Locate and identify every blood parasite.
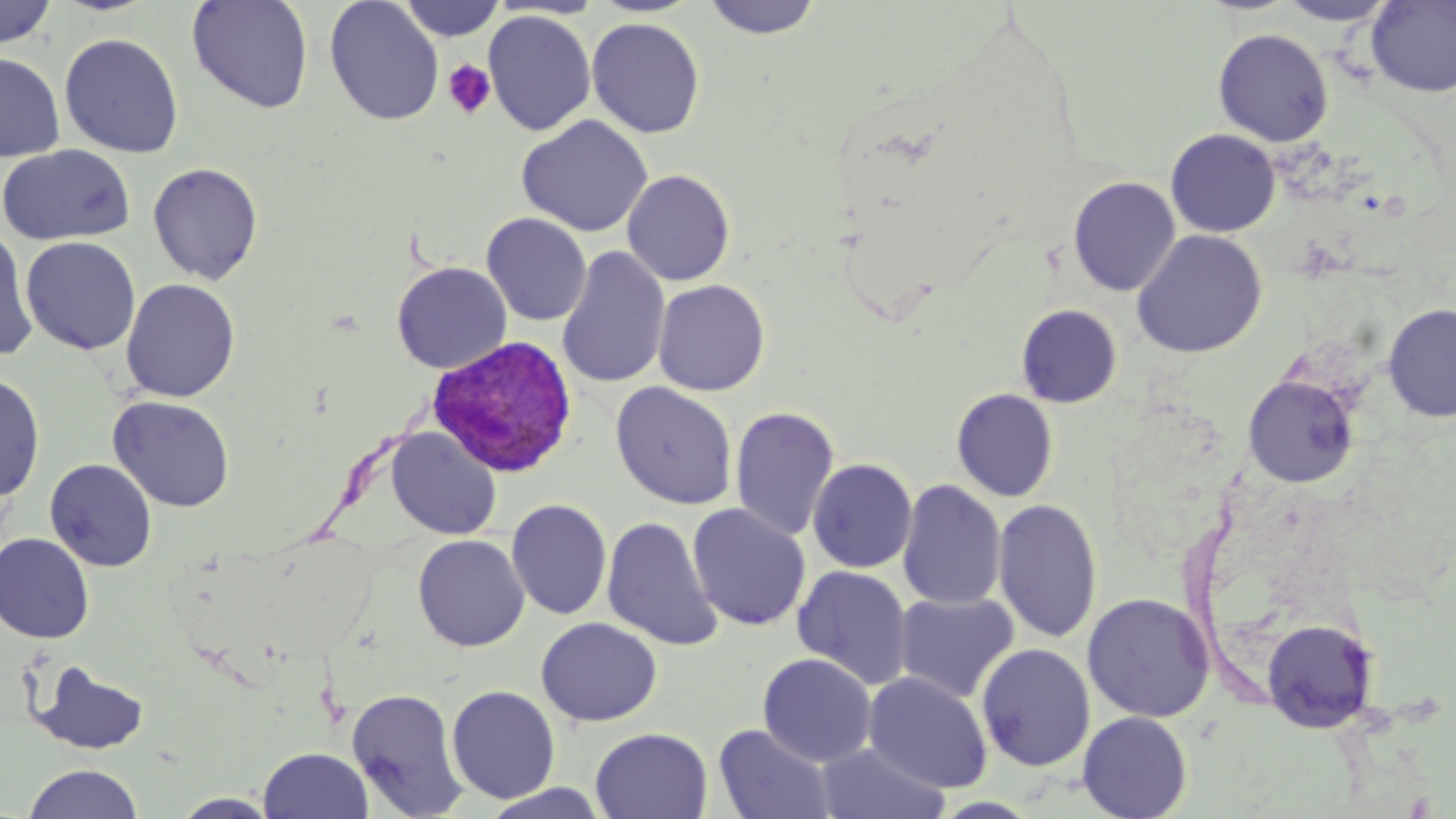

Approximate bounding boxes as named x1/y1/x2/y2 corners in pixels.
Plasmodium vivax-infected red blood cells: (x1=426, y1=335, x2=579, y2=478).
No Plasmodium falciparum, Plasmodium ovale, Plasmodium malariae, Babesia divergens, or Trypanosoma brucei observed.

Summary:
  - Uninfected red blood cell locations: (x1=186, y1=0, x2=314, y2=115), (x1=323, y1=0, x2=445, y2=127), (x1=396, y1=0, x2=507, y2=42), (x1=701, y1=0, x2=824, y2=40), (x1=0, y1=1, x2=57, y2=50), (x1=1277, y1=1, x2=1397, y2=26), (x1=1366, y1=1, x2=1456, y2=98), (x1=483, y1=10, x2=596, y2=136), (x1=586, y1=17, x2=705, y2=138), (x1=1212, y1=28, x2=1334, y2=146), (x1=59, y1=33, x2=184, y2=158), (x1=0, y1=51, x2=66, y2=162), (x1=516, y1=115, x2=653, y2=237), (x1=1165, y1=129, x2=1281, y2=237), (x1=0, y1=144, x2=135, y2=246), (x1=147, y1=162, x2=263, y2=284), (x1=622, y1=170, x2=735, y2=286), (x1=1067, y1=177, x2=1181, y2=296), (x1=481, y1=213, x2=592, y2=326), (x1=504, y1=223, x2=647, y2=345), (x1=0, y1=225, x2=39, y2=362), (x1=1131, y1=229, x2=1268, y2=359), (x1=21, y1=236, x2=141, y2=355), (x1=557, y1=247, x2=671, y2=389), (x1=391, y1=261, x2=512, y2=374), (x1=120, y1=279, x2=241, y2=402), (x1=652, y1=279, x2=770, y2=396), (x1=1381, y1=303, x2=1456, y2=423), (x1=1016, y1=304, x2=1123, y2=408), (x1=0, y1=373, x2=45, y2=503), (x1=1242, y1=374, x2=1359, y2=488), (x1=610, y1=382, x2=738, y2=510), (x1=951, y1=389, x2=1059, y2=502), (x1=107, y1=395, x2=235, y2=513), (x1=730, y1=406, x2=840, y2=542), (x1=385, y1=427, x2=501, y2=540), (x1=807, y1=458, x2=917, y2=573), (x1=44, y1=459, x2=158, y2=572), (x1=897, y1=481, x2=1007, y2=611), (x1=506, y1=498, x2=613, y2=621), (x1=992, y1=498, x2=1102, y2=644), (x1=686, y1=503, x2=811, y2=632), (x1=601, y1=515, x2=723, y2=653), (x1=0, y1=533, x2=95, y2=643), (x1=412, y1=534, x2=530, y2=652), (x1=792, y1=566, x2=914, y2=690), (x1=893, y1=592, x2=1019, y2=704), (x1=1082, y1=593, x2=1215, y2=723), (x1=535, y1=617, x2=662, y2=727), (x1=1261, y1=619, x2=1380, y2=733), (x1=976, y1=643, x2=1095, y2=772), (x1=757, y1=653, x2=877, y2=767), (x1=31, y1=660, x2=151, y2=755), (x1=863, y1=671, x2=993, y2=793), (x1=446, y1=685, x2=561, y2=804), (x1=347, y1=687, x2=469, y2=817), (x1=1077, y1=711, x2=1193, y2=819), (x1=713, y1=724, x2=835, y2=819), (x1=590, y1=727, x2=713, y2=818), (x1=814, y1=742, x2=950, y2=819), (x1=258, y1=747, x2=373, y2=819), (x1=23, y1=763, x2=144, y2=819), (x1=477, y1=783, x2=613, y2=817), (x1=170, y1=792, x2=283, y2=818)
  - Platelet locations: (x1=442, y1=60, x2=496, y2=120)
  - Slide-level diagnosis: Plasmodium vivax
  - Image size: 1456×819 pixels
  - Modality: optical microscopy
  - Field of view: single
  - Magnification: 1000x
  - Stain: May-Grünwald-Giemsa
  - Preparation: thin blood smear